Assess this cell for malaria.
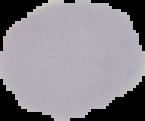
Uninfected.

Summary:
  - Image size: 145×121 pixels
  - Preparation: thin blood film
  - Image type: cell region segmented out of the field of view; surrounding area masked to black